Comment on the morphology of the erythrocytes.
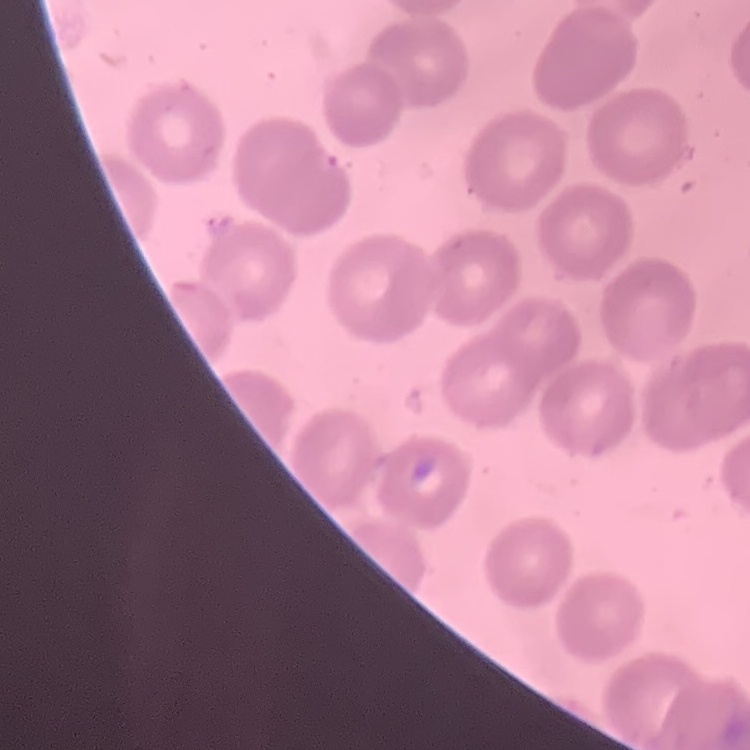

No rouleaux formation.

preparation = thin peripheral smear
stain = Field's or Giemsa
image type = one tile cut from a larger photomicrograph